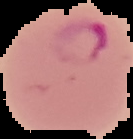
Summary:
  - Preparation: thin blood film
  - Malaria status: parasitized
  - Image type: cell region segmented out of the field of view; surrounding area masked to black
  - Image size: 133×139 pixels